Outline each blood parasite and name the species.
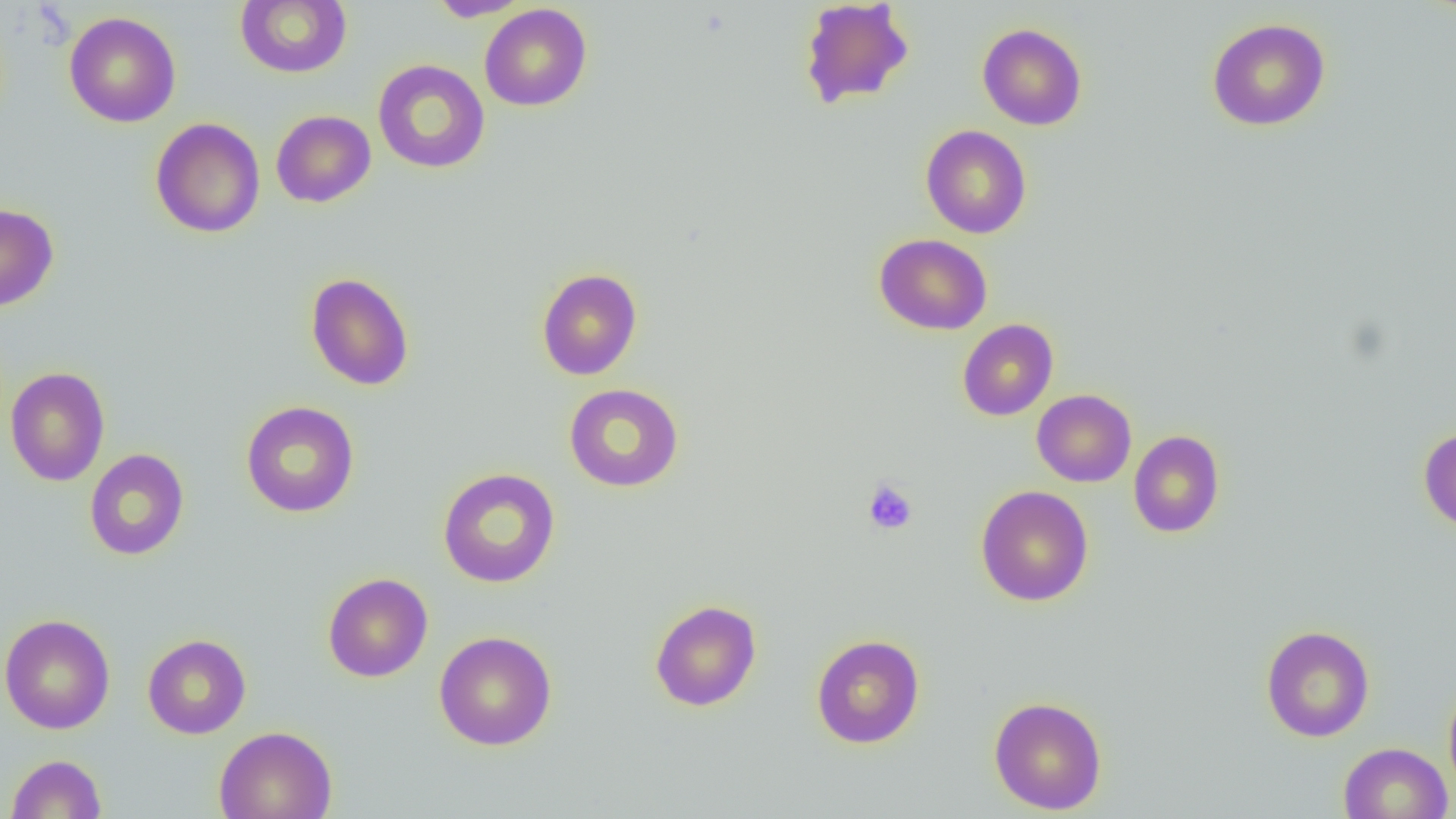

No blood parasites observed.

slide-level diagnosis = no evidence of blood parasites
preparation = thin blood smear
magnification = 1000x
modality = optical microscopy
uninfected red blood cell locations = approximate bounding boxes as named x1/y1/x2/y2 corners in pixels: (x1=235, y1=0, x2=352, y2=78), (x1=426, y1=0, x2=531, y2=22), (x1=799, y1=0, x2=915, y2=110), (x1=479, y1=4, x2=592, y2=111), (x1=64, y1=11, x2=181, y2=127), (x1=1206, y1=18, x2=1331, y2=131), (x1=977, y1=23, x2=1088, y2=130), (x1=373, y1=60, x2=490, y2=173), (x1=271, y1=110, x2=376, y2=208), (x1=150, y1=117, x2=266, y2=238), (x1=920, y1=124, x2=1032, y2=238), (x1=0, y1=202, x2=59, y2=311), (x1=874, y1=233, x2=992, y2=335), (x1=536, y1=268, x2=643, y2=380), (x1=305, y1=272, x2=414, y2=391), (x1=957, y1=319, x2=1058, y2=420), (x1=5, y1=366, x2=110, y2=487), (x1=564, y1=383, x2=685, y2=492), (x1=1032, y1=389, x2=1137, y2=487), (x1=240, y1=400, x2=360, y2=518), (x1=1418, y1=426, x2=1456, y2=533), (x1=1129, y1=430, x2=1225, y2=538), (x1=84, y1=448, x2=189, y2=561), (x1=437, y1=467, x2=561, y2=588), (x1=976, y1=485, x2=1094, y2=607), (x1=322, y1=572, x2=433, y2=682), (x1=649, y1=599, x2=762, y2=711), (x1=0, y1=613, x2=115, y2=735), (x1=1260, y1=625, x2=1375, y2=742), (x1=433, y1=631, x2=557, y2=751), (x1=811, y1=633, x2=925, y2=748), (x1=142, y1=634, x2=251, y2=739), (x1=1443, y1=678, x2=1456, y2=802), (x1=988, y1=695, x2=1107, y2=814), (x1=214, y1=725, x2=338, y2=819), (x1=1338, y1=742, x2=1453, y2=819), (x1=6, y1=753, x2=107, y2=818)
image size = 1456×819 pixels
field of view = one of a larger specimen
platelet locations = approximate bounding boxes as named x1/y1/x2/y2 corners in pixels: (x1=863, y1=479, x2=918, y2=535)